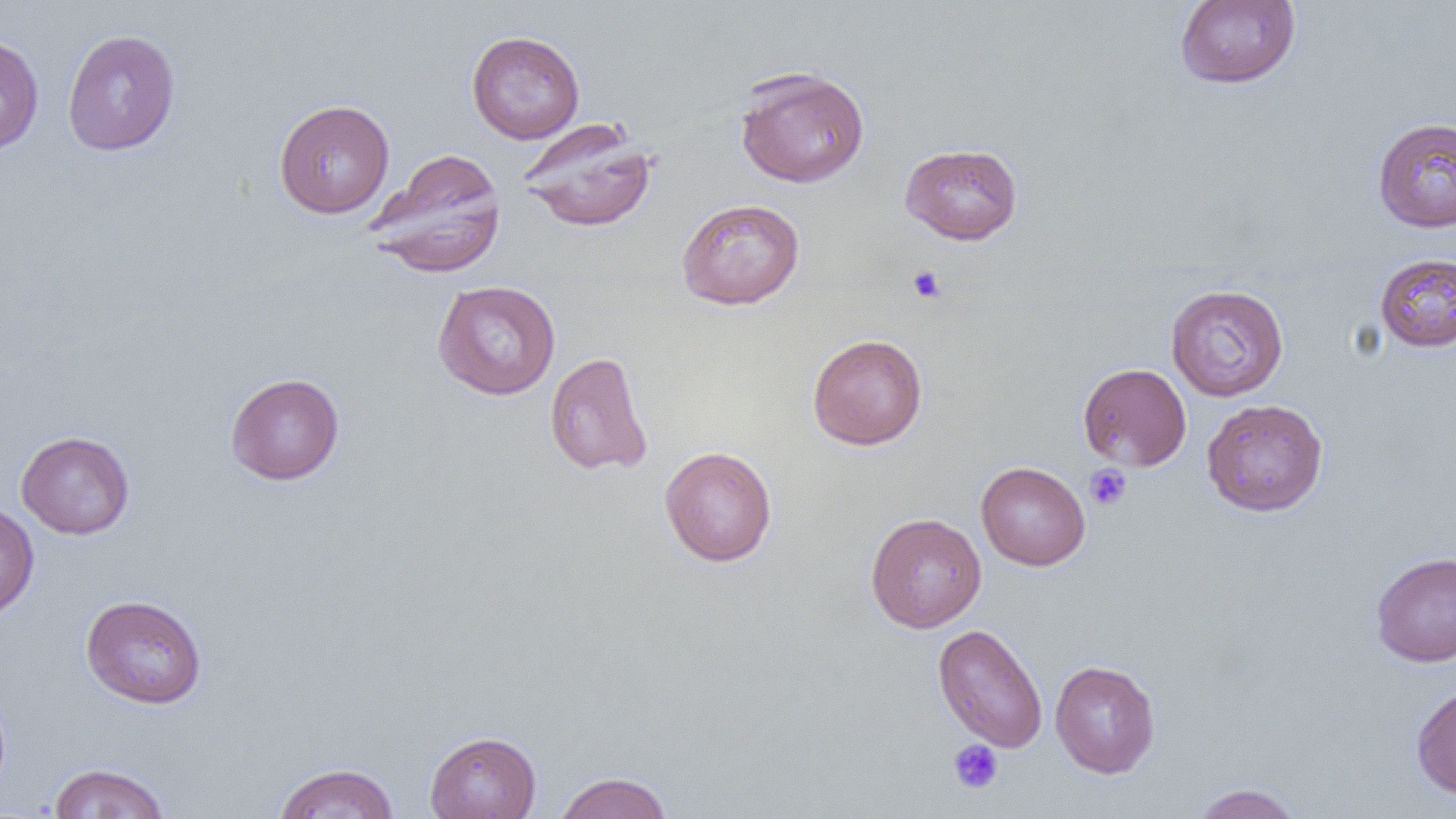

{
  "slide_level_diagnosis": "negative for blood parasites",
  "field_of_view": "one of a larger specimen",
  "platelet_locations": "approximate bounding boxes as named x1/y1/x2/y2 corners in pixels: (x1=907, y1=265, x2=946, y2=303), (x1=1085, y1=464, x2=1132, y2=511), (x1=949, y1=740, x2=1003, y2=794)",
  "uninfected_red_blood_cell_locations": "approximate bounding boxes as named x1/y1/x2/y2 corners in pixels: (x1=1175, y1=0, x2=1300, y2=89), (x1=62, y1=29, x2=180, y2=156), (x1=466, y1=29, x2=585, y2=144), (x1=0, y1=34, x2=44, y2=155), (x1=735, y1=65, x2=870, y2=188), (x1=274, y1=98, x2=395, y2=218), (x1=1373, y1=117, x2=1456, y2=233), (x1=518, y1=119, x2=657, y2=232), (x1=899, y1=143, x2=1023, y2=244), (x1=367, y1=150, x2=506, y2=279), (x1=676, y1=198, x2=805, y2=310), (x1=1374, y1=253, x2=1456, y2=352), (x1=432, y1=280, x2=561, y2=400), (x1=1166, y1=283, x2=1289, y2=401), (x1=807, y1=333, x2=928, y2=450), (x1=544, y1=351, x2=653, y2=476), (x1=1078, y1=363, x2=1192, y2=471), (x1=225, y1=372, x2=344, y2=485), (x1=1202, y1=398, x2=1328, y2=516), (x1=16, y1=430, x2=135, y2=539), (x1=659, y1=445, x2=777, y2=567), (x1=976, y1=461, x2=1090, y2=570), (x1=0, y1=502, x2=40, y2=621), (x1=865, y1=512, x2=987, y2=633), (x1=1371, y1=551, x2=1456, y2=667), (x1=81, y1=594, x2=207, y2=708), (x1=933, y1=624, x2=1048, y2=752), (x1=1050, y1=660, x2=1160, y2=778), (x1=1411, y1=683, x2=1456, y2=800), (x1=425, y1=730, x2=541, y2=818), (x1=272, y1=762, x2=399, y2=819), (x1=48, y1=763, x2=171, y2=818), (x1=553, y1=771, x2=674, y2=819), (x1=1190, y1=783, x2=1303, y2=819)",
  "magnification": "1000x",
  "modality": "light microscopy",
  "preparation": "thin blood smear",
  "image_size": "1456×819 pixels"
}